Describe the morphology of the erythrocytes.
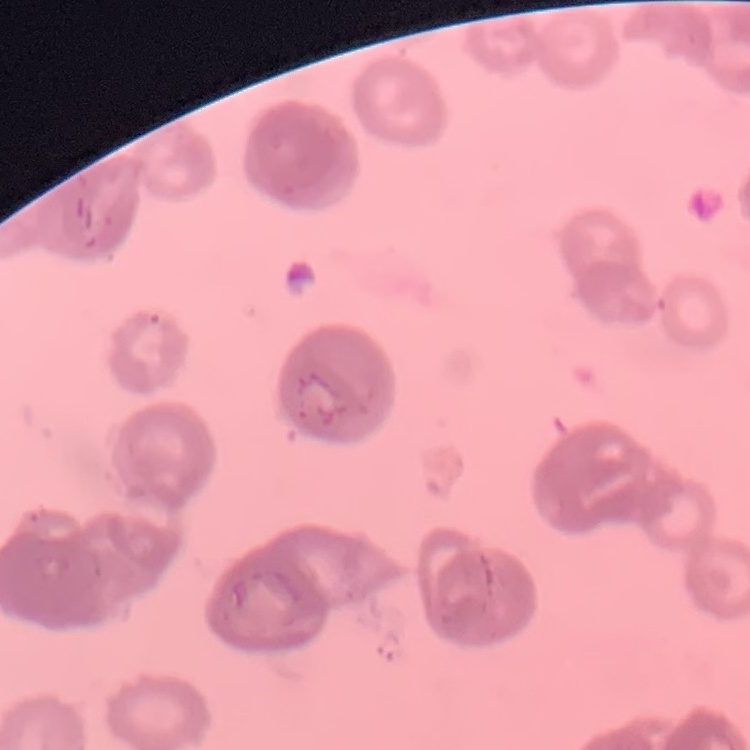

They show rouleaux formation.

Thin peripheral smear. Stained with either Field's or Giemsa. Square crop of a larger photomicrograph.